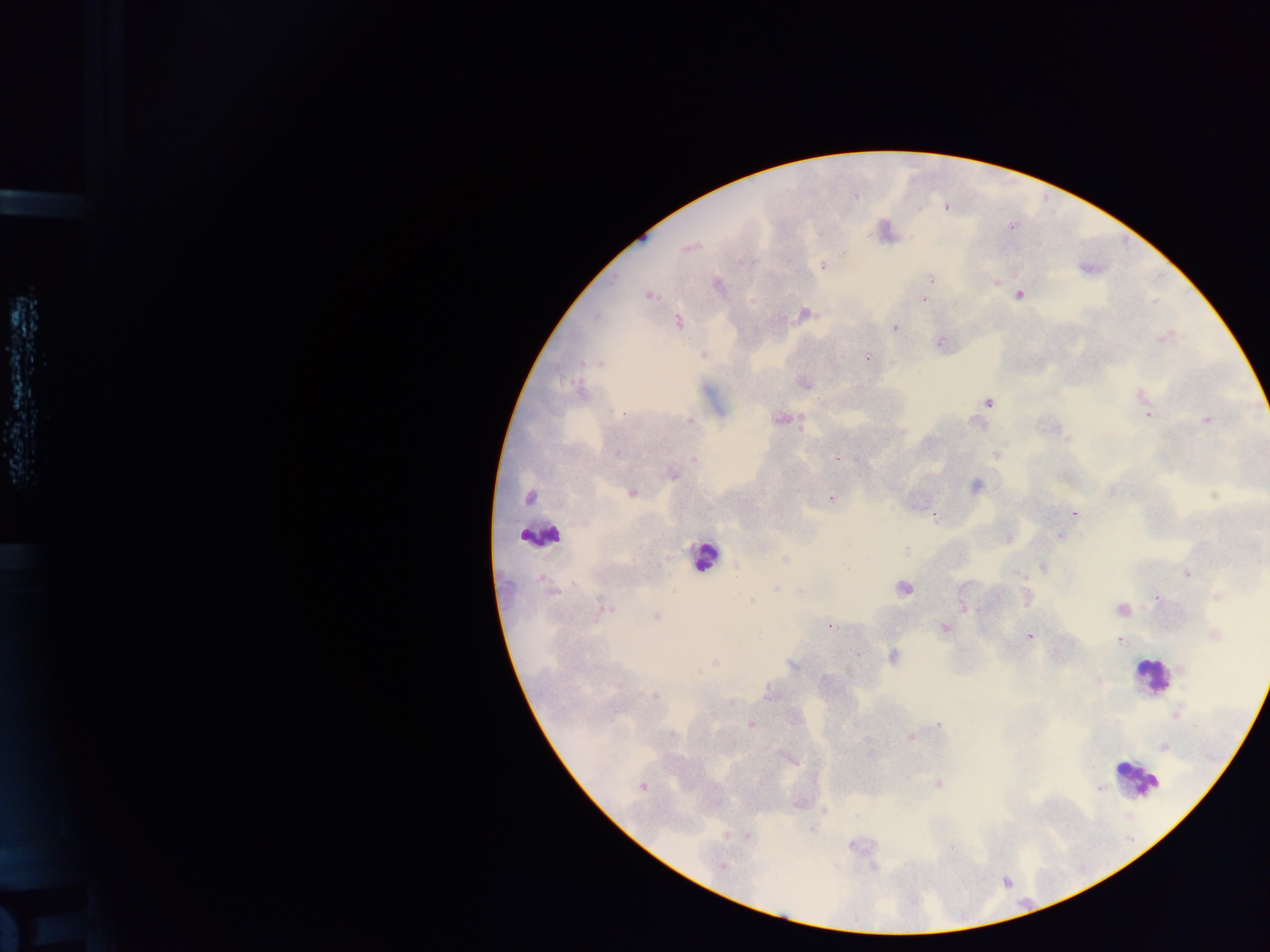
Approximate centers as (x, y) in pixels. Leukocyte locations: (540, 534), (704, 556), (1151, 676), (1137, 778). Plasmodium parasite locations: (855, 195), (946, 207), (1012, 226), (689, 247), (844, 253), (746, 262), (822, 265), (930, 278), (995, 283), (717, 285), (1018, 294), (648, 295), (923, 299), (804, 314), (678, 322), (895, 327), (1166, 336), (940, 342), (703, 355), (867, 357), (600, 364), (804, 384), (1139, 395), (988, 402), (623, 413), (1148, 415), (780, 419), (1206, 420), (689, 421), (977, 423), (801, 427), (1066, 436), (618, 453), (996, 454), (836, 458), (694, 459), (672, 475), (975, 485), (632, 493), (1215, 495), (528, 498), (831, 499), (1074, 514), (935, 515), (1060, 536), (1008, 539), (784, 559), (735, 565), (1043, 567), (1186, 574), (1020, 575), (541, 578), (903, 588), (776, 589), (551, 593), (997, 597), (1156, 597), (1217, 597), (1027, 598), (751, 601), (964, 609), (603, 610), (1121, 610), (656, 617), (830, 626), (944, 627), (1214, 635), (1029, 636), (1119, 641), (892, 656), (714, 663), (793, 665), (1183, 670), (825, 679), (1099, 682), (770, 694), (655, 696), (1177, 714), (750, 724), (940, 724), (671, 734), (910, 736), (1164, 748), (939, 785), (642, 786), (1098, 788), (725, 834), (747, 836), (723, 866). Collected in Ghana. Image is 1270×952 pixels. Single field of view. Mobile-phone photograph taken through the microscope. Thick blood film.